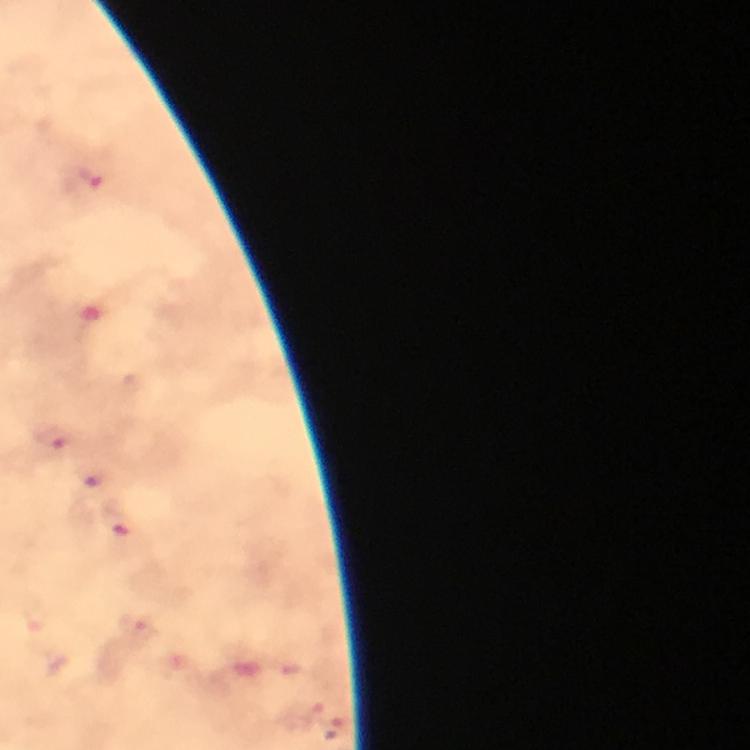 Approximate centers as {x, y} in pixels. Malaria parasite locations: {92, 178}, {55, 440}, {98, 482}, {119, 525}, {142, 633}, {314, 717}, {339, 727}. Image is 750×750 pixels. Cropped region of a single field of view. Immersion oil was used. At 100x magnification. From a malaria diagnostic workup. Smartphone photograph taken through a microscope. Thick blood film. Giemsa-stained preparation.